State the blood parasite species.
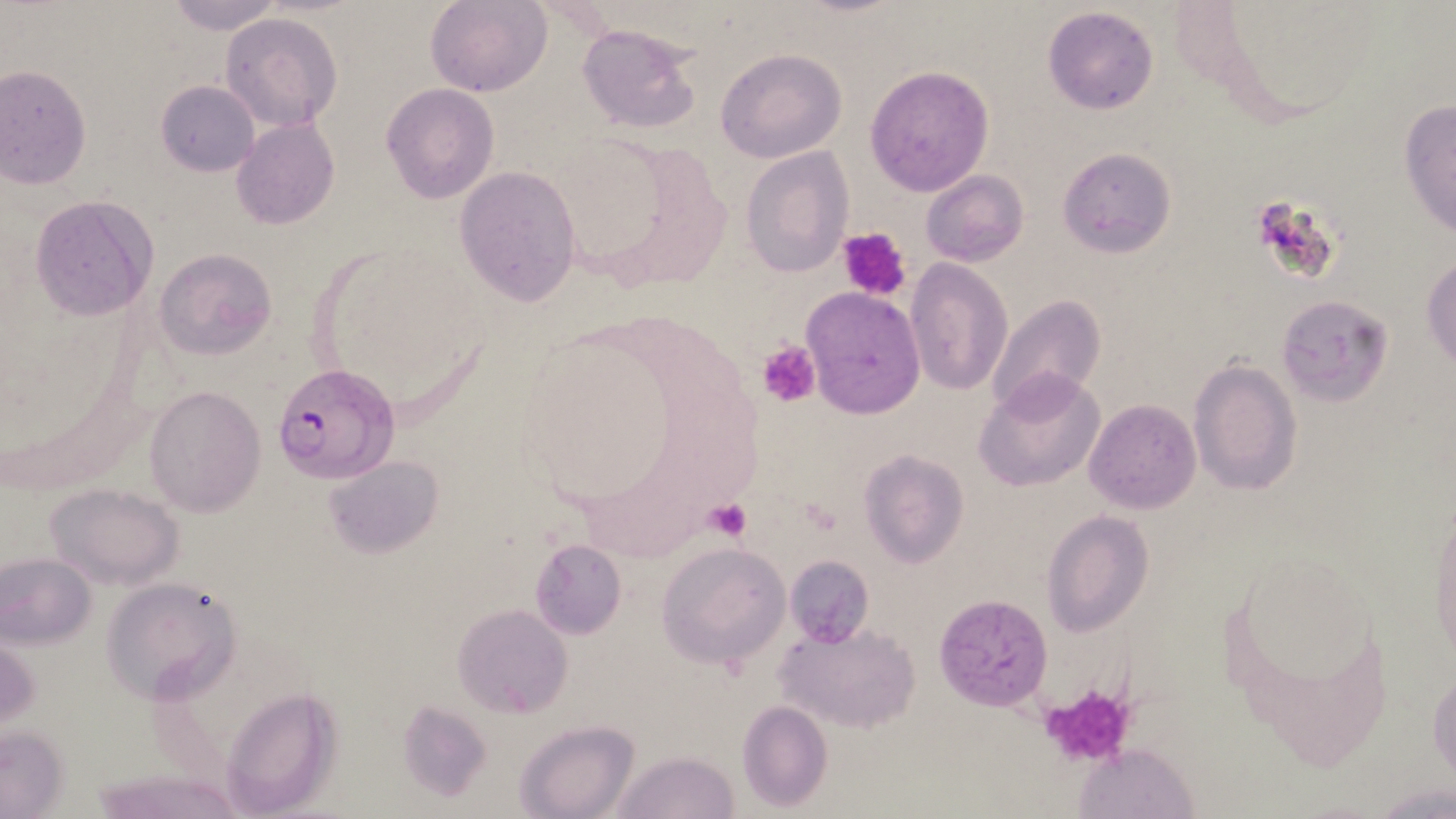

Plasmodium falciparum.

field of view = single
Plasmodium falciparum-infected red blood cell locations = approximate bounding boxes as named x1/y1/x2/y2 corners in pixels: (x1=273, y1=361, x2=398, y2=484)
magnification = 1000x
image size = 1456×819 pixels
modality = optical microscopy
uninfected red blood cell locations = approximate bounding boxes as named x1/y1/x2/y2 corners in pixels: (x1=162, y1=0, x2=287, y2=34), (x1=427, y1=1, x2=550, y2=96), (x1=1041, y1=6, x2=1160, y2=114), (x1=219, y1=11, x2=342, y2=132), (x1=575, y1=22, x2=701, y2=133), (x1=716, y1=47, x2=846, y2=164), (x1=864, y1=64, x2=994, y2=197), (x1=0, y1=65, x2=92, y2=188), (x1=154, y1=80, x2=259, y2=178), (x1=382, y1=83, x2=499, y2=204), (x1=1398, y1=96, x2=1456, y2=240), (x1=230, y1=119, x2=341, y2=231), (x1=1057, y1=146, x2=1176, y2=258), (x1=739, y1=147, x2=854, y2=278), (x1=454, y1=165, x2=582, y2=306), (x1=921, y1=169, x2=1029, y2=267), (x1=30, y1=195, x2=159, y2=320), (x1=153, y1=249, x2=276, y2=361), (x1=1422, y1=252, x2=1455, y2=370), (x1=905, y1=259, x2=1011, y2=395), (x1=800, y1=288, x2=924, y2=417), (x1=1275, y1=294, x2=1391, y2=405), (x1=986, y1=295, x2=1105, y2=414), (x1=1189, y1=360, x2=1301, y2=497), (x1=976, y1=371, x2=1105, y2=492), (x1=144, y1=385, x2=267, y2=516), (x1=1084, y1=398, x2=1200, y2=514), (x1=859, y1=450, x2=969, y2=568), (x1=323, y1=455, x2=442, y2=558), (x1=45, y1=482, x2=186, y2=589), (x1=1427, y1=494, x2=1456, y2=672), (x1=1042, y1=510, x2=1152, y2=637), (x1=529, y1=538, x2=627, y2=640), (x1=655, y1=542, x2=790, y2=668), (x1=0, y1=552, x2=96, y2=650), (x1=784, y1=555, x2=874, y2=648), (x1=102, y1=574, x2=244, y2=702), (x1=933, y1=594, x2=1054, y2=711), (x1=454, y1=604, x2=573, y2=717), (x1=775, y1=621, x2=922, y2=734), (x1=1428, y1=665, x2=1455, y2=790), (x1=218, y1=686, x2=340, y2=814), (x1=736, y1=699, x2=832, y2=812), (x1=396, y1=701, x2=491, y2=801), (x1=514, y1=721, x2=640, y2=819), (x1=1, y1=728, x2=68, y2=817), (x1=1075, y1=744, x2=1198, y2=819), (x1=610, y1=750, x2=740, y2=819)
platelet locations = approximate bounding boxes as named x1/y1/x2/y2 corners in pixels: (x1=838, y1=226, x2=913, y2=300), (x1=758, y1=340, x2=820, y2=407), (x1=705, y1=499, x2=753, y2=543), (x1=1035, y1=682, x2=1140, y2=765)
stain = May-Grünwald-Giemsa
preparation = thin blood smear